Outline each Plasmodium ovale-infected red blood cell.
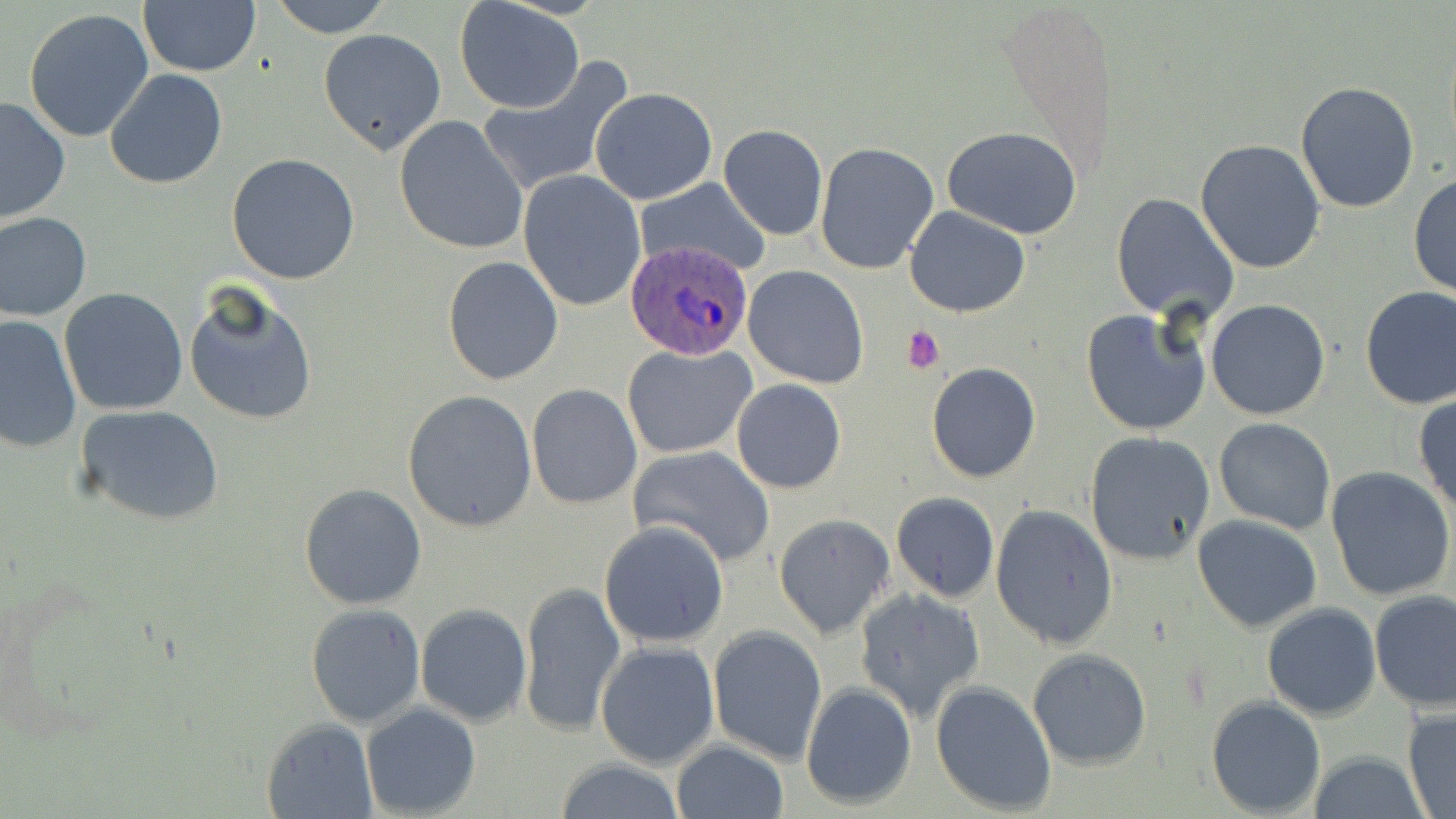

Approximate bounding boxes as (x1,y1)-(x2,y2) corner pairs in pixels.
Plasmodium ovale-infected red blood cells: (625,237)-(758,361).

Platelet locations: (902,325)-(946,374). Uninfected red blood cell locations: (269,0)-(394,37), (454,0)-(586,116), (138,2)-(261,77), (24,8)-(155,144), (318,27)-(448,156), (474,58)-(636,198), (104,68)-(230,190), (1295,80)-(1420,213), (589,88)-(717,205), (0,95)-(72,226), (393,115)-(529,257), (719,124)-(828,239), (941,127)-(1082,240), (1194,139)-(1326,273), (813,142)-(940,274), (226,153)-(361,285), (516,168)-(646,311), (1410,174)-(1456,299), (633,176)-(772,277), (1110,193)-(1239,321), (902,206)-(1030,319), (0,212)-(92,321), (442,256)-(564,387), (743,265)-(870,389), (182,285)-(318,428), (1359,286)-(1456,410), (58,287)-(188,417), (1206,300)-(1331,420), (1081,308)-(1210,436), (0,313)-(82,455), (621,342)-(756,459), (927,363)-(1041,483), (731,377)-(846,494), (525,382)-(642,509), (402,390)-(538,532), (1414,394)-(1456,517), (75,403)-(225,527), (1213,418)-(1337,534), (1084,431)-(1215,565), (627,443)-(775,567), (1326,467)-(1456,600), (297,483)-(427,610), (891,492)-(999,603), (990,503)-(1119,651), (772,514)-(895,640), (1193,514)-(1323,633), (598,521)-(729,647), (518,580)-(624,738), (853,588)-(987,725), (1369,590)-(1455,712), (1261,601)-(1382,720), (415,602)-(532,728), (305,604)-(424,727), (707,625)-(829,765), (594,640)-(721,771), (1026,647)-(1152,770), (930,680)-(1058,814), (801,682)-(919,811), (1206,696)-(1327,817), (360,702)-(483,818), (1402,704)-(1456,817), (260,717)-(377,818), (670,740)-(791,819), (1309,750)-(1428,819), (552,758)-(686,817). Slide-level diagnosis: Plasmodium ovale. Single field of view. Light microscopy. Captured at 1000x magnification. Thin blood film. Image is 1456×819 pixels. May-Grünwald-Giemsa-stained preparation.